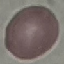
Malaria status: uninfected. Thin blood smear. Automatically extracted cell patch, resized to 64 × 64 pixels. Photographed with a smartphone camera at the microscope eyepiece. Giemsa-stained preparation.